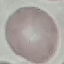

{
  "result": "negative for malaria parasites",
  "preparation": "thin blood film",
  "capture": "smartphone through the microscope eyepiece",
  "image_type": "automatically extracted cell patch, resized to 64 × 64 pixels",
  "stain": "Giemsa"
}